State the preparation type.
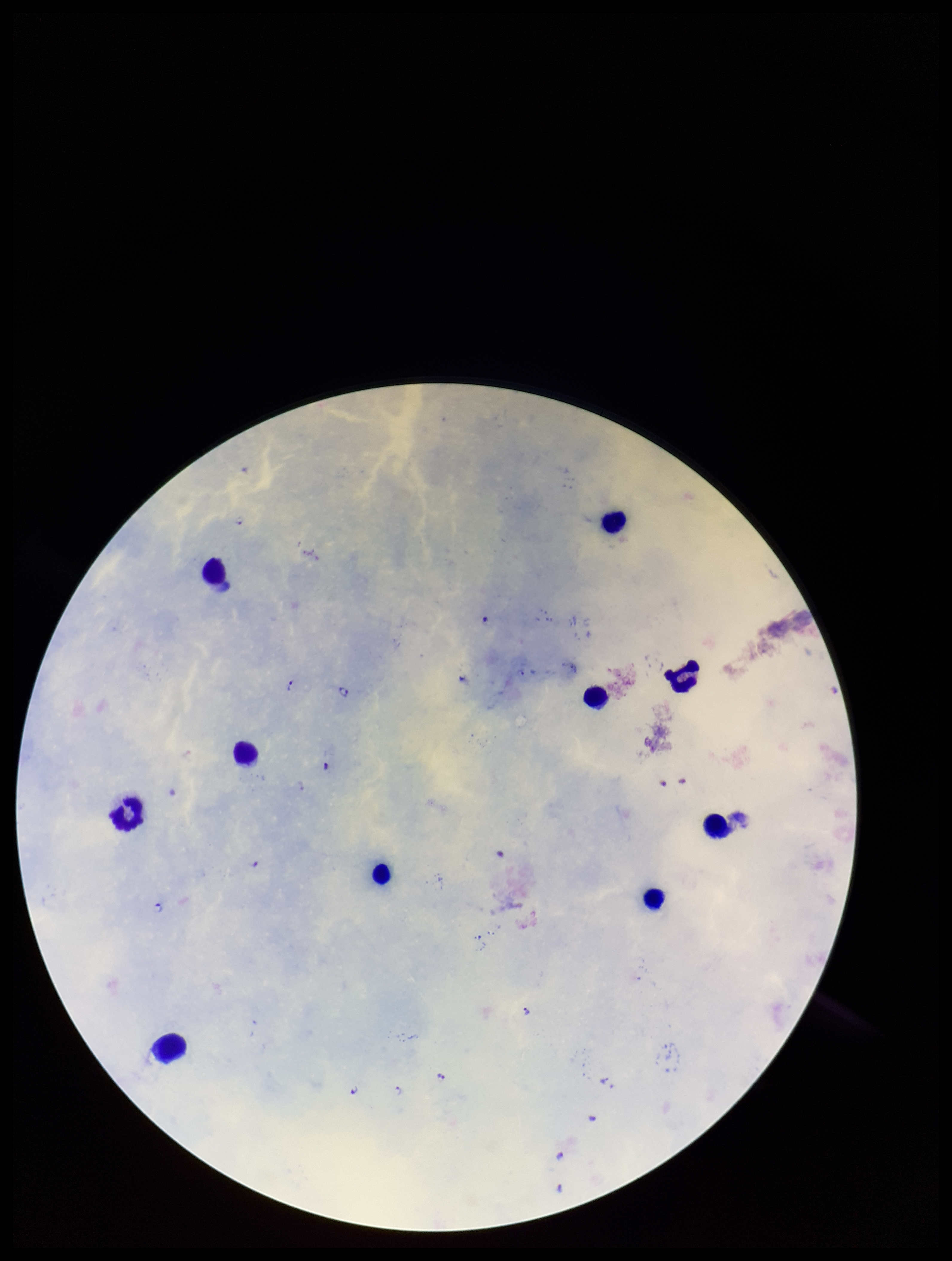

Thick.

Summary:
  - Image size: 952×1261 pixels
  - Parasite count: 12
  - Patient malaria status: positive
  - Species reported for this patient: Plasmodium falciparum
  - Field of view: single
  - Plasmodium parasites: seen
  - Capture: smartphone photograph through the microscope eyepiece
  - Stain: Giemsa
  - Leukocyte count: 10